Assess this cell for malaria.
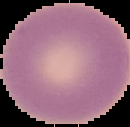

It is uninfected.

preparation = thin blood smear
image type = cell region segmented out of the field of view; surrounding area masked to black
image size = 130×127 pixels